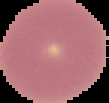 From a thin blood smear. The area outside the segmented cell region is set to black. Image is 109×103 pixels. Result: no Plasmodium parasites seen.